Classify this cell by malaria status.
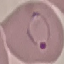
Parasitized.

Thin smear of blood. Photographed with a smartphone camera at the microscope eyepiece. Automatically extracted cell patch, resized to 64 × 64 pixels. Giemsa stain.